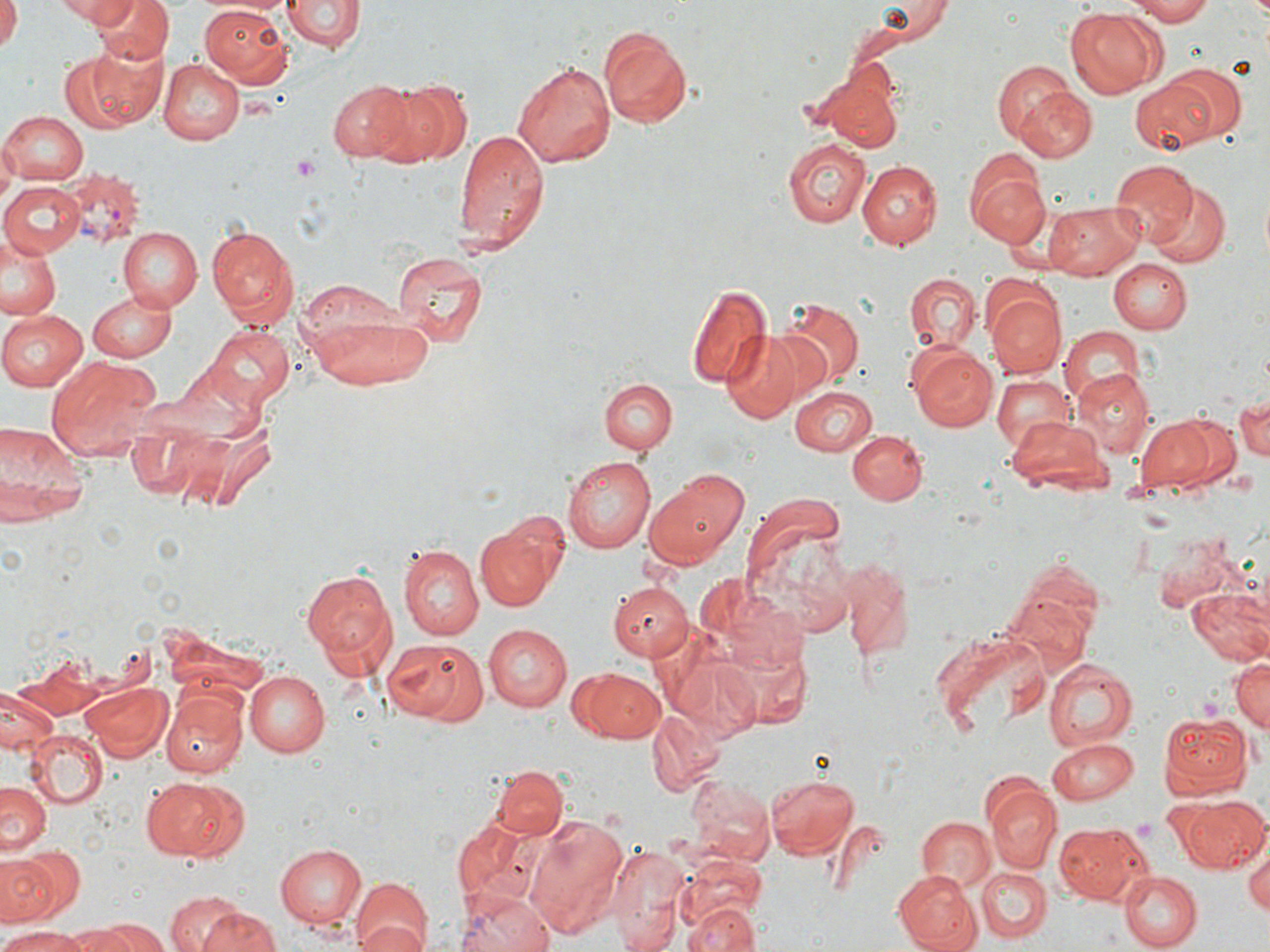
Summary:
  - Coordinate format: approximate bounding boxes as (x1, y1, x2, y2) in pixels
  - Plasmodium vivax-infected red blood cell locations: (64, 167, 147, 244)
  - Platelet locations: (292, 155, 320, 179), (1133, 817, 1161, 842)
  - Uninfected red blood cell locations: (1, 0, 21, 53), (52, 0, 131, 24), (94, 0, 172, 66), (281, 0, 363, 52), (870, 0, 953, 43), (1122, 0, 1215, 24), (198, 1, 292, 84), (1067, 7, 1162, 97), (599, 25, 696, 128), (64, 45, 163, 132), (158, 57, 243, 145), (512, 59, 616, 167), (992, 60, 1078, 149), (1159, 64, 1245, 144), (815, 76, 903, 152), (375, 77, 471, 167), (328, 78, 420, 162), (1130, 78, 1220, 156), (1010, 85, 1097, 165), (1, 110, 88, 184), (452, 126, 549, 253), (0, 139, 17, 210), (783, 139, 870, 227), (857, 160, 939, 248), (1109, 160, 1195, 246), (968, 166, 1048, 247), (0, 180, 85, 259), (1149, 183, 1229, 267), (1043, 202, 1146, 280), (204, 224, 298, 329), (119, 226, 203, 309), (0, 232, 62, 323), (391, 248, 487, 347), (339, 259, 476, 370), (1107, 259, 1192, 332), (904, 273, 981, 353), (297, 283, 436, 388), (686, 283, 772, 390), (983, 286, 1065, 377), (87, 290, 179, 360), (779, 299, 863, 385), (0, 309, 87, 391), (202, 323, 294, 412), (1059, 325, 1145, 403), (719, 328, 809, 421), (909, 342, 1001, 431), (49, 355, 161, 457), (990, 371, 1075, 454), (1076, 371, 1155, 457), (600, 378, 678, 453), (790, 385, 878, 455), (1231, 392, 1270, 464), (1177, 415, 1240, 487), (1137, 416, 1214, 490), (1005, 417, 1107, 489), (0, 423, 88, 525), (848, 429, 927, 505), (563, 454, 655, 552), (642, 474, 749, 568), (741, 492, 855, 631), (474, 523, 557, 612), (400, 546, 484, 640), (1009, 556, 1107, 651), (835, 558, 916, 662), (302, 565, 397, 677), (609, 584, 694, 663), (1186, 588, 1270, 668), (482, 624, 573, 711), (931, 630, 1051, 739), (381, 639, 489, 725), (1229, 654, 1269, 736), (1042, 657, 1137, 749), (573, 667, 666, 741), (246, 671, 330, 756), (79, 680, 174, 762), (0, 685, 61, 758), (163, 689, 246, 778), (646, 708, 728, 798), (1159, 711, 1254, 797), (28, 731, 107, 806), (1046, 738, 1141, 803), (492, 763, 568, 840), (764, 771, 860, 858), (687, 774, 775, 864), (142, 777, 245, 862), (0, 781, 51, 858), (983, 782, 1063, 869), (1181, 794, 1268, 873), (522, 815, 629, 941), (916, 816, 995, 891), (455, 818, 545, 908), (1055, 820, 1150, 905), (274, 843, 367, 932), (610, 843, 692, 952), (1245, 845, 1270, 918), (0, 848, 83, 929), (676, 856, 767, 937), (977, 868, 1051, 944), (892, 869, 980, 952), (1122, 871, 1201, 950), (348, 878, 431, 952), (454, 891, 554, 952), (165, 892, 246, 952), (683, 900, 761, 952), (197, 907, 283, 952), (353, 917, 427, 952), (97, 918, 166, 952), (64, 925, 143, 952), (1, 929, 88, 952)
  - Slide-level diagnosis: Plasmodium vivax
  - Image size: 1270×952 pixels
  - Field of view: single
  - Modality: optical microscopy
  - Preparation: thin blood smear
  - Stain: May-Grünwald-Giemsa
  - Magnification: 1000x